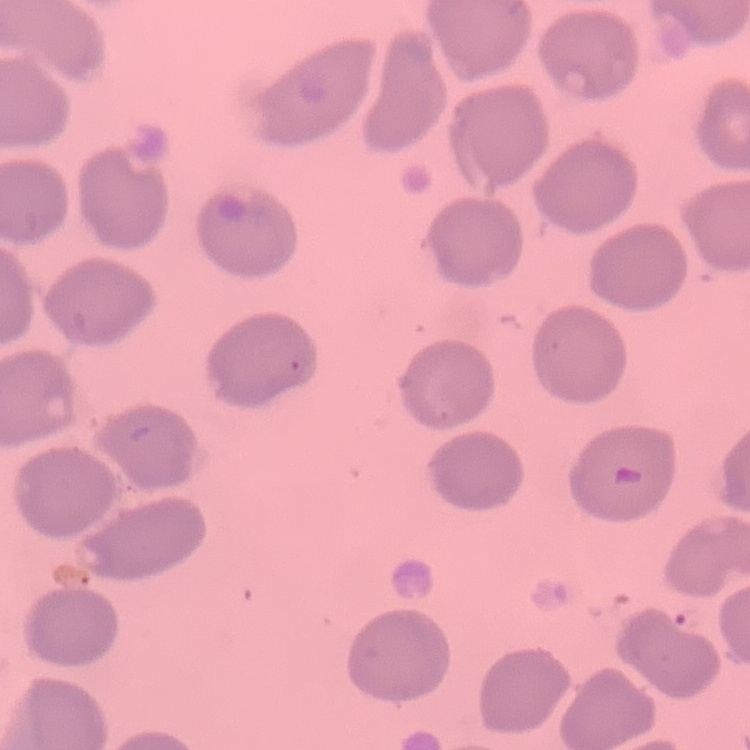

The red blood cells exhibit no rouleaux formation. Field's or Giemsa stain. Thin blood smear. One tile cut from a larger photomicrograph.